Locate every leukocyte (white blood cell).
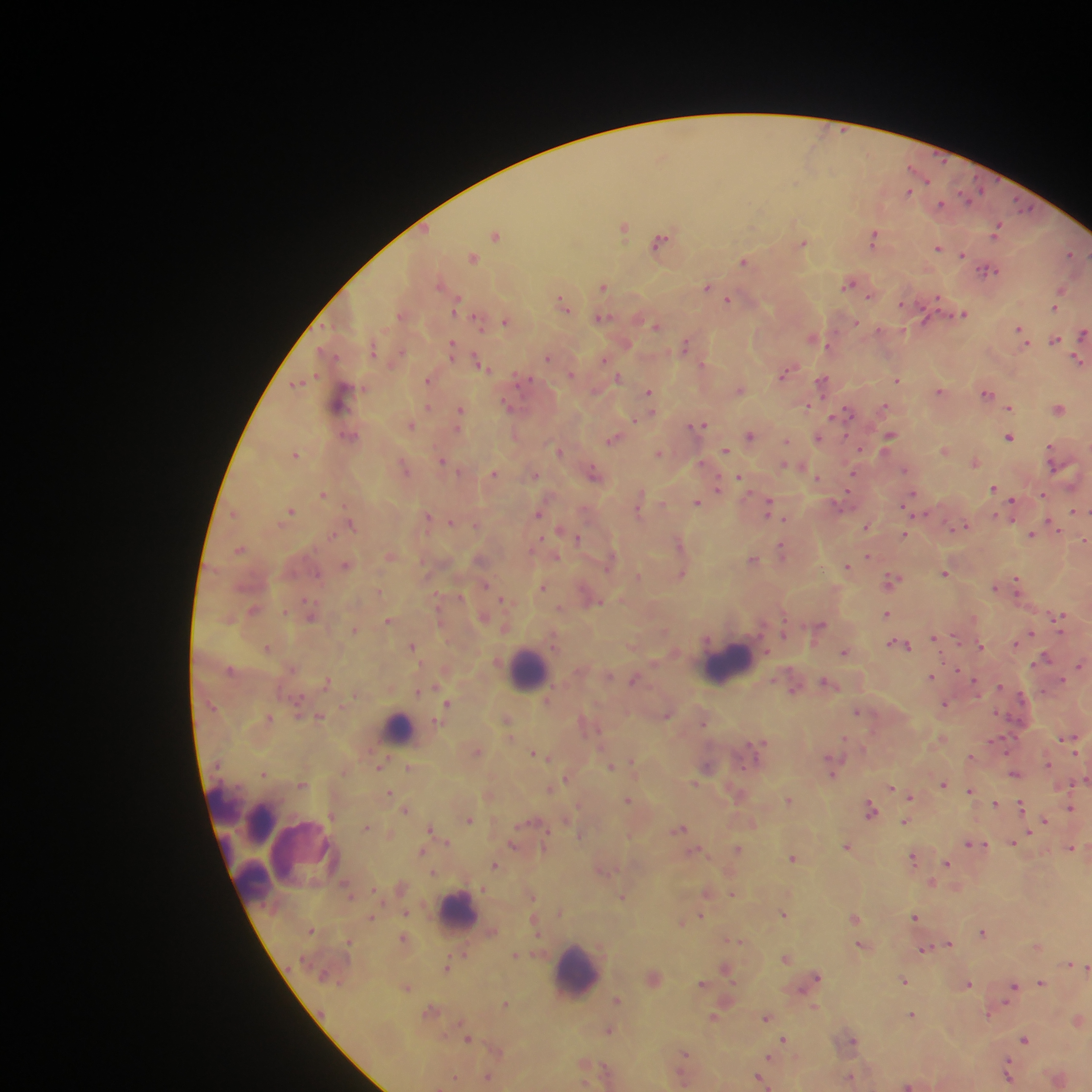

Approximate centers as (x, y) in pixels.
Leukocytes: (730, 663), (529, 670), (398, 728), (224, 805), (260, 823), (284, 837), (304, 852), (252, 882), (459, 911), (576, 970).

malaria_parasite_locations: 'approximate centers as (x, y) in pixels: (909, 191), (941, 205), (624, 226), (996, 227), (495, 234), (874, 236), (660, 242), (803, 243), (938, 247), (963, 253), (1071, 254), (473, 256), (745, 261), (988, 270), (442, 284), (850, 284), (604, 285), (708, 287), (1061, 291), (719, 292), (729, 298), (564, 303), (1055, 307), (963, 313), (403, 314), (601, 317), (478, 320), (506, 320), (855, 322), (656, 324), (1022, 332), (1083, 333), (815, 338), (1056, 339), (687, 344), (452, 348), (548, 357), (604, 359), (1077, 360), (482, 365), (788, 372), (618, 378), (429, 380), (897, 380), (823, 381), (297, 383), (740, 390), (940, 391), (987, 391), (649, 392), (341, 398), (808, 405), (511, 406), (1010, 406), (884, 407), (1060, 408), (460, 412), (844, 412), (411, 425), (698, 425), (750, 435), (350, 436), (890, 436), (1009, 436), (818, 437), (613, 439), (787, 440), (946, 450), (558, 451), (726, 451), (1051, 451), (659, 452), (296, 453), (443, 461), (975, 461), (788, 465), (797, 465), (405, 467), (493, 472), (595, 473), (534, 474), (852, 476), (817, 477), (741, 478), (717, 487), (994, 489), (324, 494), (1044, 494), (912, 495), (698, 502), (841, 505), (1013, 505), (639, 506), (769, 507), (290, 511), (539, 511), (1075, 511), (234, 513), (925, 514), (428, 517), (451, 521), (351, 522), (867, 526), (964, 526), (1054, 527), (565, 532), (904, 534), (1033, 534), (576, 537), (1084, 540), (680, 546), (241, 548), (783, 550), (869, 555), (391, 556), (753, 559), (610, 561), (345, 565), (847, 566), (945, 572), (681, 573), (638, 576), (892, 579), (1016, 583), (543, 587), (995, 587), (503, 598), (592, 598), (254, 610), (310, 612), (886, 614), (484, 617), (1059, 617), (390, 621), (819, 625), (354, 629), (1029, 634), (936, 639), (1018, 642), (900, 644), (412, 645), (981, 645), (268, 647), (845, 652), (1046, 658), (1080, 664), (932, 677), (635, 679), (328, 680), (828, 683), (793, 689), (419, 691), (547, 701), (448, 703), (945, 703), (857, 711), (320, 716), (269, 718), (507, 720), (1069, 739), (762, 743), (476, 751), (537, 755), (545, 756), (971, 757), (634, 763), (1048, 763), (611, 765), (380, 766), (409, 767), (707, 767), (834, 767), (264, 772), (1015, 773), (566, 777), (1085, 780), (695, 783), (302, 784), (943, 784), (551, 788), (893, 788), (971, 790), (390, 791), (737, 792), (488, 795), (910, 796), (628, 800), (790, 800), (996, 803), (1020, 805), (1071, 807), (406, 809), (872, 810), (469, 820), (906, 820), (1045, 820), (752, 822), (367, 827), (431, 828), (680, 828), (580, 834), (1013, 842), (515, 844), (975, 844), (847, 846), (1071, 847), (738, 849), (421, 851), (696, 851), (794, 856), (914, 858), (947, 862), (495, 865), (602, 870), (434, 872), (932, 884), (708, 892), (732, 893), (532, 896), (622, 896), (406, 911), (784, 913), (701, 916), (372, 917), (855, 917), (915, 917), (535, 921), (682, 923), (983, 932), (405, 938), (734, 939), (948, 944), (862, 945), (1037, 945), (926, 949), (515, 955), (787, 957), (1071, 965), (1081, 966), (447, 967), (1086, 967), (726, 968), (654, 979), (813, 979), (904, 979), (1042, 982), (703, 984), (968, 984), (1013, 986), (407, 987), (617, 1000), (506, 1003), (815, 1007), (433, 1010), (991, 1012), (912, 1015), (714, 1016), (766, 1016), (1078, 1020), (610, 1029), (468, 1038), (1025, 1038), (784, 1039), (852, 1039), (497, 1050), (685, 1056), (770, 1057), (1009, 1072), (682, 1074), (488, 1076), (455, 1077), (852, 1077), (761, 1078), (1059, 1078), (908, 1084)'
field_of_view: single
image_size: 1092×1092 pixels
capture: mobile-phone photograph through a microscope
country: Ghana
preparation: thick blood smear